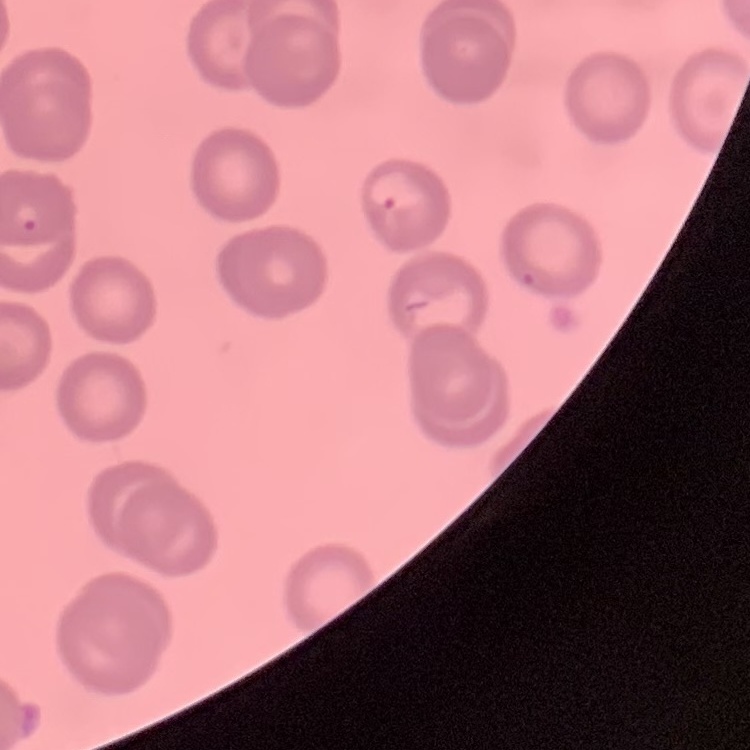
Summary:
  - Red blood cell morphology: no rouleaux formation
  - Preparation: thin peripheral smear
  - Stain: Field's or Giemsa
  - Image type: square crop of a larger photomicrograph